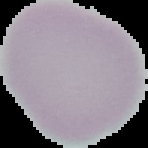

image size = 148×148 pixels
preparation = thin blood film
malaria status = uninfected
image type = segmented cell region on a black background